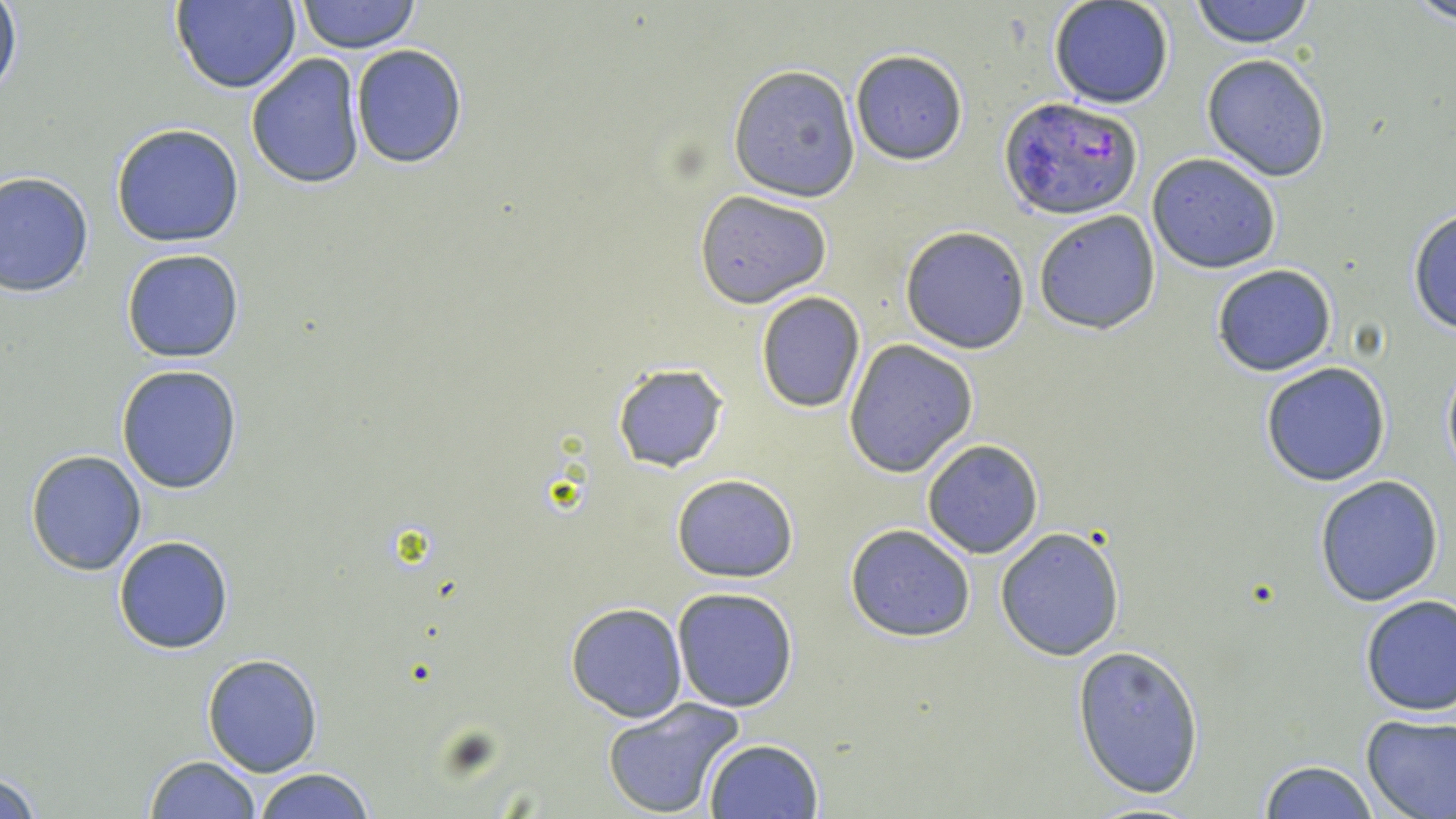
Approximate bounding boxes as (x1, y1, x2, y2) in pixels. Plasmodium falciparum-infected red blood cell locations: (1000, 95, 1144, 223). Uninfected red blood cell locations: (297, 0, 420, 53), (1191, 0, 1315, 48), (1411, 0, 1456, 25), (169, 1, 302, 93), (1048, 1, 1176, 109), (0, 2, 22, 103), (350, 44, 467, 168), (850, 50, 966, 165), (246, 53, 365, 189), (1202, 54, 1331, 181), (727, 65, 862, 201), (110, 123, 245, 247), (1147, 153, 1282, 273), (0, 170, 95, 297), (693, 189, 831, 308), (1407, 207, 1456, 334), (1033, 209, 1163, 335), (901, 225, 1031, 353), (120, 248, 244, 363), (1211, 263, 1337, 377), (754, 292, 866, 412), (844, 340, 976, 477), (1440, 357, 1456, 479), (1260, 362, 1391, 485), (611, 363, 728, 473), (115, 364, 242, 494), (921, 439, 1044, 559), (25, 449, 147, 576), (671, 473, 799, 583), (1314, 476, 1445, 607), (845, 523, 977, 641), (994, 526, 1127, 661), (114, 535, 234, 655), (671, 588, 799, 713), (1358, 593, 1455, 716), (566, 602, 689, 722), (1072, 643, 1205, 799), (202, 653, 323, 775), (603, 698, 746, 817), (1360, 711, 1456, 819), (702, 738, 823, 819), (143, 753, 261, 819), (1258, 759, 1381, 818), (0, 767, 44, 818), (250, 767, 379, 819), (1076, 799, 1210, 818). Slide-level diagnosis: Plasmodium falciparum. Image is 1456×819 pixels. May-Grünwald-Giemsa-stained preparation. One field of a larger specimen. Captured at 1000x magnification. Thin blood smear. Optical microscopy.